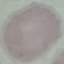
Summary:
  - Malaria status: uninfected
  - Image type: automatically extracted cell patch, resized to 64 × 64 pixels
  - Capture: smartphone camera at the microscope eyepiece
  - Preparation: thin blood smear
  - Stain: Giemsa